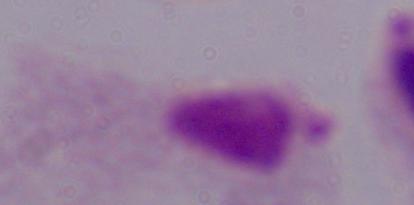

{
  "identification": "trichomonad",
  "modality": "photomicrograph",
  "magnification": "1000x"
}